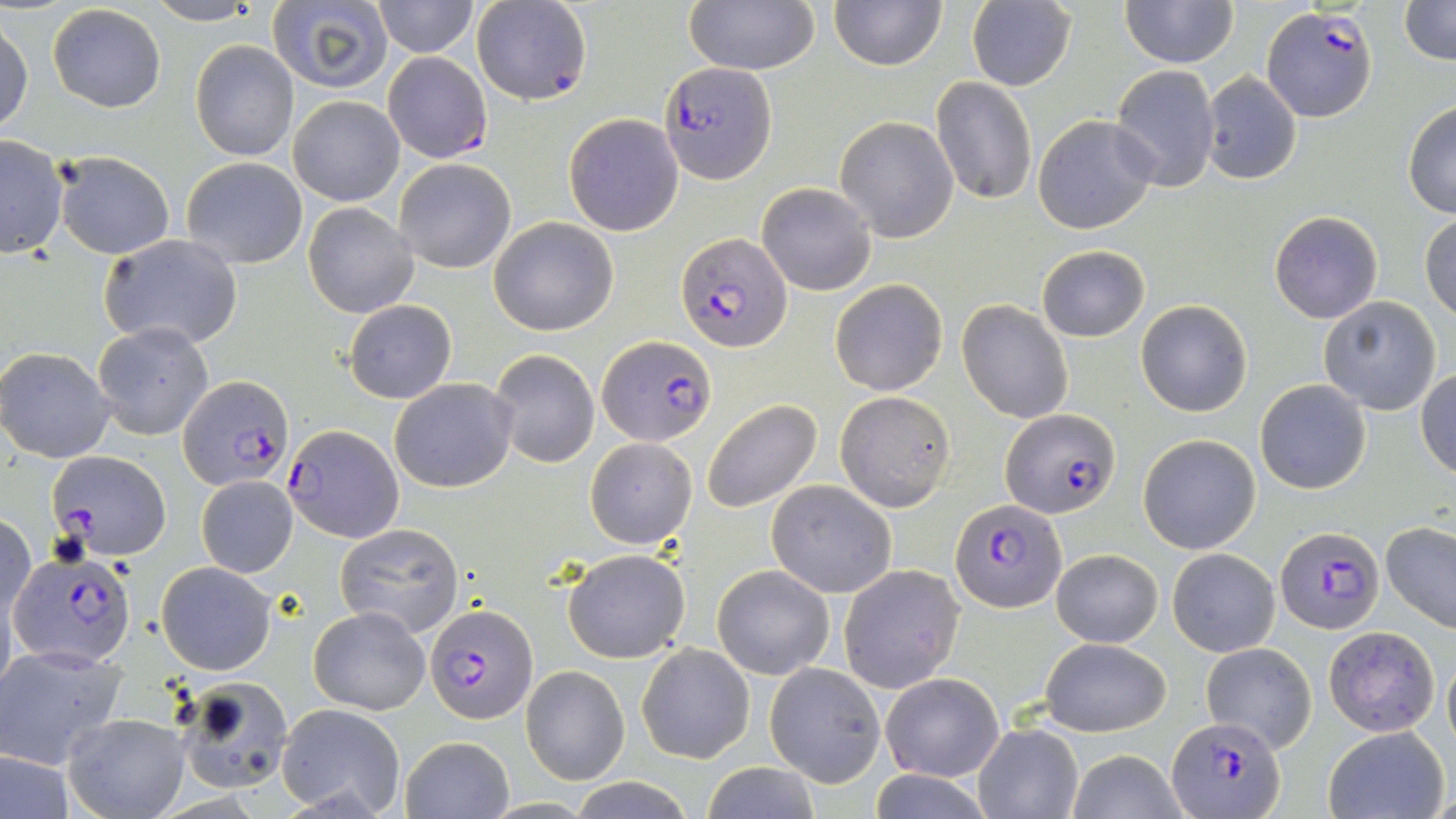 Approximate bounding boxes as (x1, y1, x2, y2) in pixels. Plasmodium falciparum-infected red blood cell locations: (1259, 5, 1377, 123), (382, 51, 493, 164), (659, 63, 776, 183), (676, 232, 793, 354), (597, 335, 718, 445), (175, 376, 292, 491), (1001, 407, 1121, 519), (284, 423, 402, 541), (48, 451, 172, 561), (950, 498, 1065, 612), (1276, 527, 1385, 634), (11, 549, 136, 667), (426, 603, 538, 723), (1166, 716, 1282, 818). Uninfected red blood cell locations: (372, 0, 478, 56), (684, 0, 821, 76), (1121, 0, 1238, 68), (1397, 0, 1456, 67), (267, 1, 394, 92), (471, 1, 593, 107), (830, 1, 946, 71), (966, 1, 1077, 91), (145, 2, 262, 25), (46, 4, 167, 113), (0, 16, 33, 136), (189, 39, 300, 163), (1110, 64, 1221, 194), (1199, 72, 1304, 185), (931, 77, 1037, 206), (288, 95, 404, 207), (1403, 102, 1456, 218), (563, 113, 684, 236), (1032, 114, 1159, 234), (834, 115, 961, 242), (0, 135, 68, 261), (53, 150, 177, 259), (180, 157, 308, 269), (394, 159, 515, 273), (756, 182, 877, 296), (302, 202, 418, 318), (1269, 211, 1383, 323), (1420, 213, 1456, 321), (489, 217, 619, 336), (98, 236, 244, 351), (1036, 245, 1151, 343), (829, 278, 948, 395), (1318, 297, 1441, 416), (956, 298, 1074, 424), (1136, 299, 1253, 417), (344, 300, 456, 403), (92, 321, 213, 440), (0, 347, 116, 462), (489, 350, 600, 467), (1416, 369, 1456, 478), (390, 378, 517, 493), (1254, 379, 1373, 496), (834, 390, 954, 512), (701, 398, 823, 515), (1139, 434, 1260, 553), (585, 437, 697, 549), (195, 475, 298, 578), (765, 481, 897, 599), (0, 511, 35, 624), (335, 522, 466, 639), (1381, 522, 1456, 633), (562, 547, 690, 663), (1052, 547, 1162, 647), (1167, 547, 1281, 657), (157, 562, 276, 675), (838, 563, 964, 693), (712, 564, 835, 679), (310, 606, 429, 715), (1322, 627, 1440, 736), (1039, 638, 1170, 737), (636, 642, 756, 765), (1201, 642, 1317, 751), (0, 646, 127, 768), (1442, 651, 1456, 752), (766, 662, 886, 788), (521, 666, 629, 785), (880, 673, 1004, 782), (173, 676, 293, 794), (276, 703, 406, 818), (63, 712, 187, 818), (974, 724, 1083, 818), (1323, 726, 1450, 819), (400, 735, 513, 818), (0, 748, 76, 819), (1065, 750, 1189, 819), (701, 763, 824, 819), (866, 771, 995, 818), (568, 778, 696, 817). Slide-level diagnosis: Plasmodium falciparum. May-Grünwald-Giemsa stain. Optical microscopy. 1000x magnification. Single field of view. Image is 1456×819 pixels. Thin blood smear.